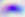
{
  "modality": "photomicrograph",
  "magnification": "400x",
  "identification": "Toxoplasma gondii"
}